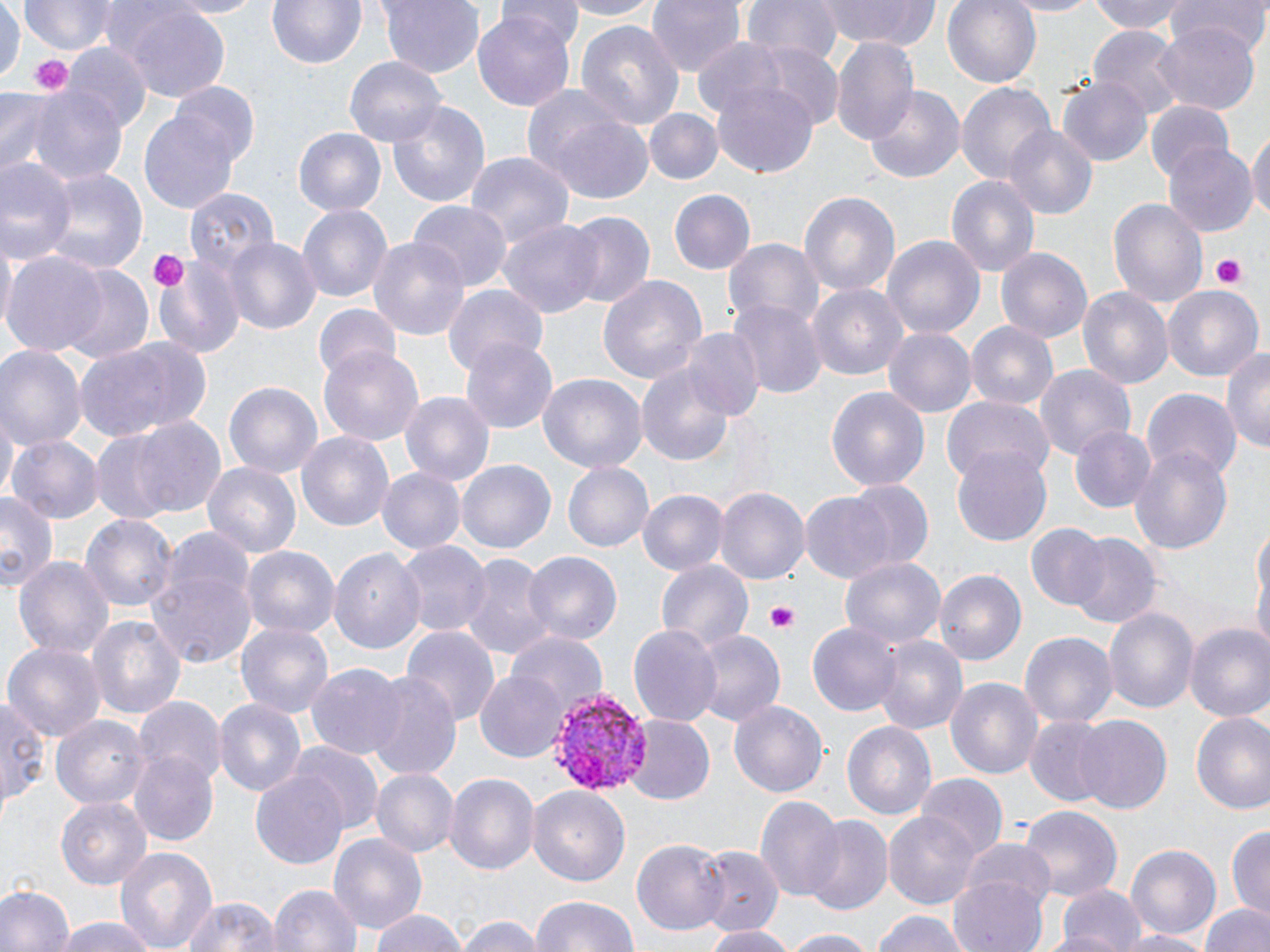
Approximate bounding boxes as [x1, y1, x2, y2] in pixels. Platelet locations: [30, 54, 72, 95], [147, 249, 189, 293], [1208, 254, 1247, 289], [766, 604, 799, 631]. Uninfected red blood cell locations: [0, 0, 21, 90], [18, 0, 120, 55], [159, 0, 267, 17], [265, 0, 369, 70], [377, 0, 486, 76], [497, 0, 581, 45], [556, 0, 666, 20], [644, 0, 745, 79], [738, 0, 844, 65], [817, 0, 941, 50], [942, 0, 1042, 90], [1001, 0, 1098, 15], [1088, 0, 1190, 35], [1167, 0, 1267, 54], [114, 2, 233, 103], [473, 10, 576, 110], [574, 21, 685, 137], [1154, 23, 1262, 114], [1089, 26, 1187, 118], [832, 37, 917, 143], [691, 38, 791, 129], [63, 42, 149, 132], [754, 42, 844, 133], [346, 56, 449, 148], [1059, 79, 1152, 166], [955, 80, 1058, 186], [172, 83, 261, 168], [711, 83, 819, 178], [864, 84, 966, 185], [24, 85, 129, 190], [0, 91, 65, 179], [384, 99, 492, 211], [1144, 100, 1234, 184], [138, 107, 241, 214], [646, 110, 721, 185], [539, 111, 656, 202], [1004, 123, 1100, 222], [293, 127, 387, 218], [1249, 131, 1270, 226], [1165, 142, 1258, 236], [464, 151, 572, 255], [1, 156, 75, 264], [37, 167, 150, 277], [946, 173, 1041, 278], [183, 188, 277, 278], [668, 190, 754, 276], [797, 190, 901, 299], [1109, 195, 1208, 308], [408, 200, 509, 294], [295, 201, 393, 302], [563, 210, 655, 307], [500, 220, 604, 318], [368, 232, 471, 341], [881, 235, 985, 338], [226, 237, 321, 336], [724, 238, 823, 333], [1, 240, 16, 337], [995, 247, 1094, 345], [2, 251, 108, 355], [152, 252, 248, 361], [57, 266, 154, 366], [598, 273, 707, 385], [807, 282, 909, 381], [1162, 283, 1264, 383], [441, 284, 549, 376], [1077, 286, 1174, 391], [729, 300, 825, 398], [312, 305, 401, 385], [964, 322, 1058, 413], [883, 327, 975, 419], [680, 328, 765, 424], [74, 336, 212, 442], [460, 337, 560, 432], [0, 343, 84, 453], [1221, 346, 1270, 454], [319, 348, 424, 446], [1033, 364, 1135, 463], [638, 365, 735, 464], [539, 374, 647, 473], [225, 381, 323, 479], [826, 385, 930, 491], [1144, 390, 1240, 481], [401, 391, 495, 488], [942, 396, 1052, 487], [2, 412, 17, 504], [129, 415, 227, 520], [1069, 425, 1157, 514], [296, 432, 396, 534], [8, 433, 103, 523], [87, 433, 185, 526], [1129, 443, 1233, 557], [952, 446, 1052, 549], [454, 459, 556, 557], [202, 460, 303, 561], [561, 462, 653, 552], [376, 468, 464, 555], [845, 478, 933, 571], [714, 486, 809, 585], [640, 489, 728, 577], [0, 491, 58, 589], [800, 491, 898, 585], [80, 512, 178, 617], [1253, 514, 1269, 636], [1027, 523, 1109, 611], [1068, 533, 1160, 631], [397, 540, 491, 641], [242, 546, 338, 641], [329, 547, 425, 657], [521, 550, 623, 645], [457, 552, 556, 664], [839, 554, 947, 648], [12, 555, 117, 662], [655, 557, 754, 653], [146, 559, 256, 669], [932, 568, 1026, 667], [1103, 606, 1198, 719], [85, 614, 185, 720], [235, 619, 336, 720], [806, 620, 902, 717], [629, 622, 722, 731], [1185, 624, 1270, 725], [402, 626, 498, 736], [693, 630, 784, 729], [505, 631, 607, 715], [1021, 633, 1117, 728], [874, 634, 968, 735], [3, 641, 105, 744], [307, 663, 408, 762], [360, 670, 464, 782], [475, 673, 566, 760], [945, 676, 1043, 783], [213, 695, 306, 799], [136, 696, 226, 787], [0, 697, 47, 814], [729, 700, 828, 797], [1190, 711, 1270, 814], [50, 714, 152, 811], [623, 715, 715, 806], [1075, 716, 1170, 816], [1026, 717, 1111, 805], [842, 719, 939, 822], [288, 742, 383, 836], [129, 751, 218, 847], [250, 769, 349, 870], [372, 769, 456, 858], [444, 773, 538, 875], [917, 776, 1006, 862], [528, 785, 629, 890], [56, 795, 152, 887], [754, 797, 845, 904], [1019, 806, 1123, 903], [884, 812, 980, 908], [805, 816, 894, 918], [1229, 826, 1270, 914], [326, 832, 427, 938], [631, 839, 729, 936], [958, 839, 1057, 919], [1124, 842, 1222, 940], [115, 845, 218, 952], [695, 846, 782, 939], [950, 875, 1050, 952], [269, 883, 362, 952], [1055, 884, 1147, 952], [0, 885, 73, 952], [528, 894, 640, 952], [179, 896, 282, 952], [1201, 900, 1269, 952], [366, 909, 473, 952], [870, 910, 974, 952], [455, 914, 545, 952], [50, 917, 163, 952], [702, 925, 799, 951], [777, 928, 885, 951], [1112, 930, 1215, 952]. Plasmodium vivax-infected red blood cell locations: [547, 688, 656, 801]. Slide-level diagnosis: Plasmodium vivax. Single field of view. Thin blood film. May-Grünwald-Giemsa stain. 1000x magnification. Image is 1270×952 pixels. Optical microscopy.